Locate every malaria parasite.
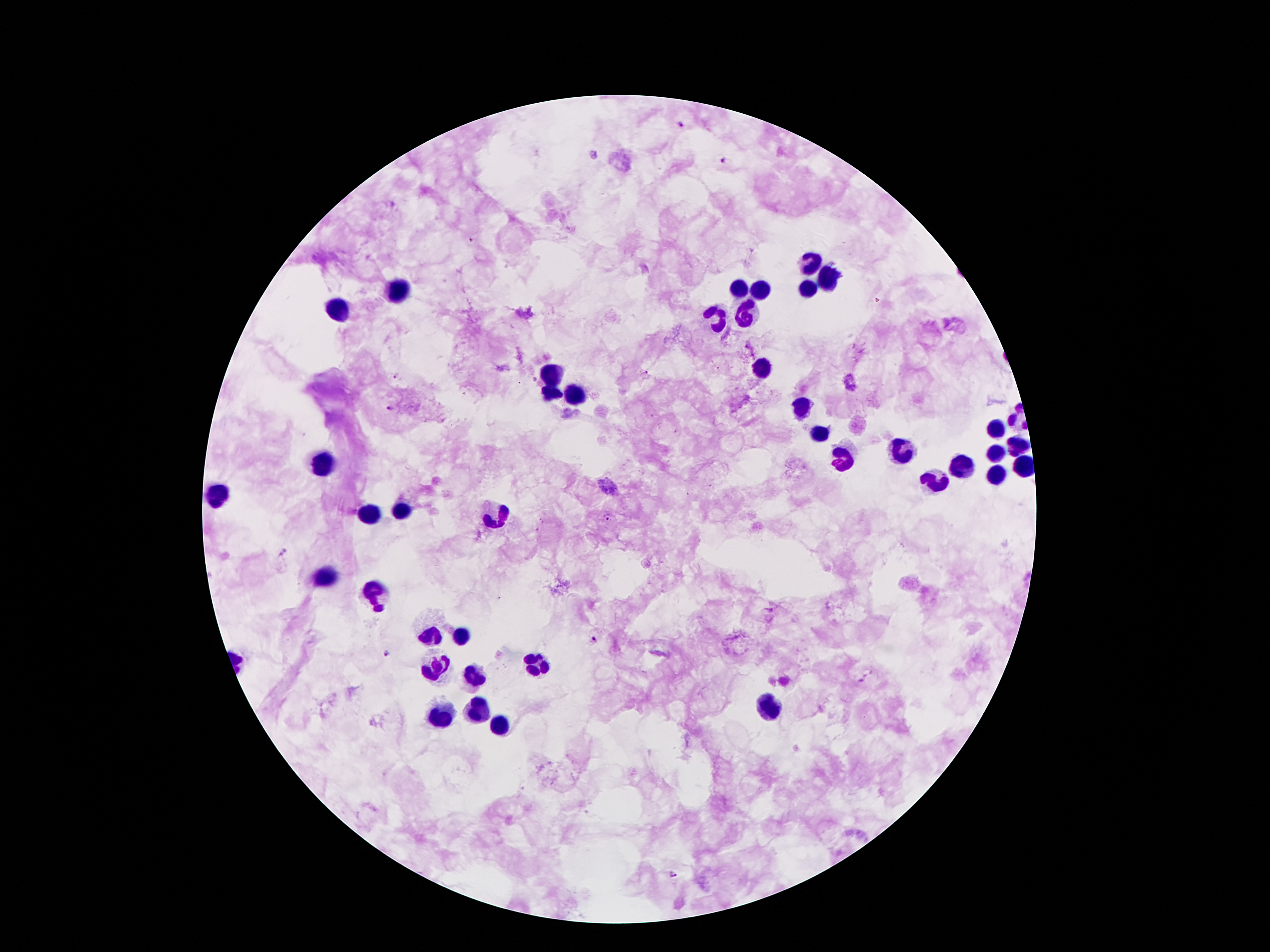
Approximate centers as [x, y] in pixels.
Malaria parasites: [679, 125], [724, 159], [643, 371], [398, 375], [391, 409], [608, 518], [282, 552], [595, 640], [388, 653], [675, 874].

Summary:
  - Leukocyte locations: [808, 261], [831, 280], [742, 286], [400, 289], [760, 289], [808, 289], [340, 307], [715, 316], [749, 316], [761, 368], [554, 373], [552, 395], [577, 395], [802, 409], [997, 429], [819, 430], [1019, 447], [899, 450], [1001, 454], [323, 461], [842, 461], [962, 466], [1022, 466], [995, 475], [938, 477], [216, 495], [404, 511], [368, 514], [495, 516], [325, 579], [374, 595], [463, 634], [432, 638], [534, 661], [434, 668], [475, 675], [769, 707], [475, 711], [440, 718], [500, 723]
  - Image size: 1270×952 pixels
  - Patient malaria status: positive for Plasmodium falciparum
  - Magnification: 100x
  - Capture: smartphone camera through the microscope eyepiece
  - Preparation: thick blood film
  - Stain: Giemsa
  - Field of view: single